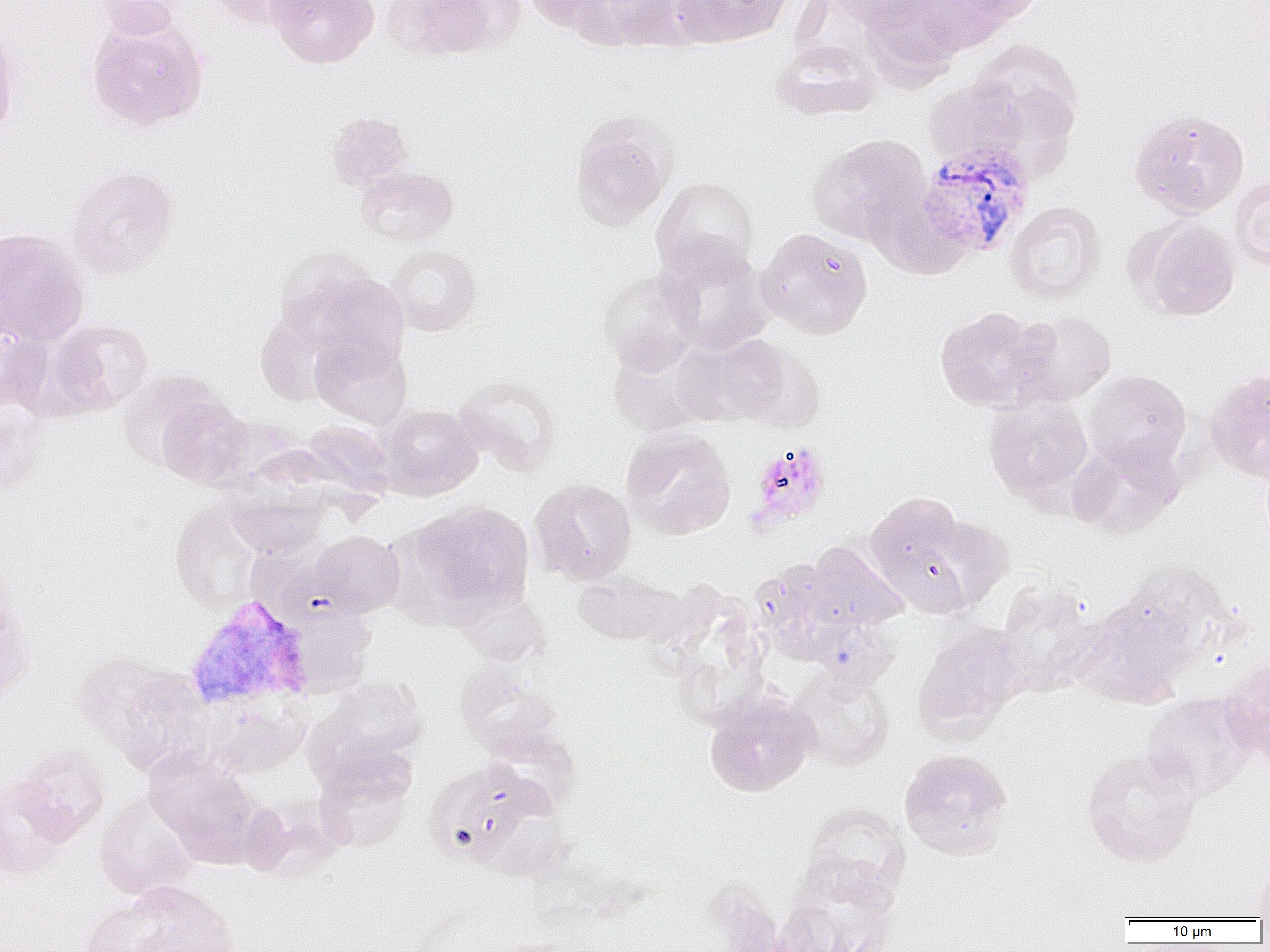

Approximate bounding boxes as (x1,y1)-(x2,y2) corner pairs in pixels. Uninfected red blood cell locations: (90,0)-(186,39), (209,0)-(315,29), (266,0)-(379,69), (382,0)-(503,59), (524,0)-(615,31), (574,0)-(686,52), (671,0)-(792,47), (830,0)-(933,30), (911,0)-(1015,55), (948,0)-(1045,25), (86,15)-(209,131), (0,23)-(21,142), (771,40)-(880,121), (968,40)-(1083,153), (923,77)-(1026,167), (1129,108)-(1249,217), (325,110)-(414,191), (569,115)-(675,231), (807,133)-(931,244), (354,165)-(459,246), (68,166)-(178,278), (1230,175)-(1270,272), (651,176)-(758,282), (1005,202)-(1106,303), (1134,218)-(1239,321), (756,227)-(873,339), (0,228)-(90,346), (657,241)-(774,354), (386,244)-(482,336), (273,245)-(388,347), (597,269)-(701,373), (304,271)-(410,366), (934,306)-(1048,411), (1008,310)-(1117,407), (0,319)-(53,414), (43,319)-(154,416), (309,332)-(413,428), (678,332)-(788,426), (719,337)-(824,432), (607,338)-(714,436), (1206,368)-(1270,482), (1084,369)-(1192,471), (118,370)-(229,473), (454,373)-(562,477), (152,392)-(254,489), (983,397)-(1093,503), (377,404)-(483,499), (0,407)-(47,494), (301,420)-(396,501), (621,428)-(737,540), (1067,437)-(1184,538), (529,477)-(637,584), (224,485)-(329,557), (865,491)-(973,609), (413,501)-(535,617), (169,503)-(266,615), (915,513)-(1015,613), (310,530)-(404,618), (807,541)-(908,630), (752,560)-(845,660), (572,570)-(681,645), (0,575)-(36,706), (996,579)-(1101,694), (455,588)-(548,666), (1076,596)-(1195,706), (913,622)-(1027,738), (72,649)-(179,752), (1221,659)-(1270,763), (454,665)-(566,759), (110,668)-(214,776), (790,668)-(895,770), (311,675)-(428,772), (704,688)-(817,798), (1142,692)-(1257,800), (199,696)-(308,777), (13,746)-(109,842), (1081,746)-(1201,866), (899,748)-(1013,861), (144,749)-(261,866), (314,749)-(417,852), (424,757)-(547,869), (0,778)-(75,877), (94,793)-(198,900), (240,797)-(341,879), (802,802)-(912,905), (780,856)-(900,952), (1250,860)-(1270,919), (115,881)-(242,952), (79,900)-(173,952). Plasmodium vivax-infected red blood cell locations: (916,142)-(1035,259), (185,594)-(314,710). Platelet locations: (746,440)-(832,533). Slide-level diagnosis: Plasmodium vivax. Thin blood smear. Optical microscopy. Single field of view. Captured at 1000x magnification. Image is 1270×952 pixels.